Comment on the morphology of the erythrocytes.
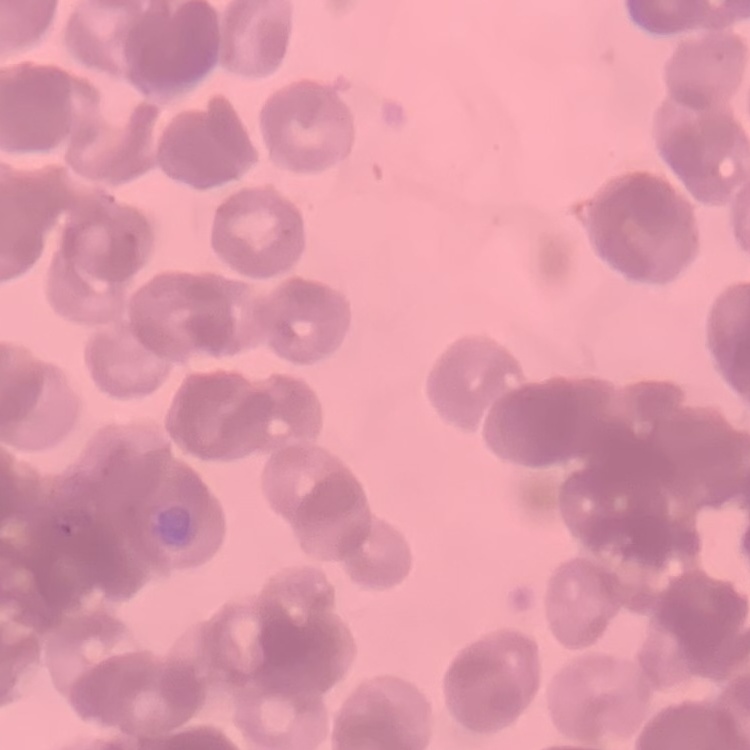
They show rouleaux formation.

Thin peripheral smear. Field's or Giemsa stain. One tile cut from a larger photomicrograph.